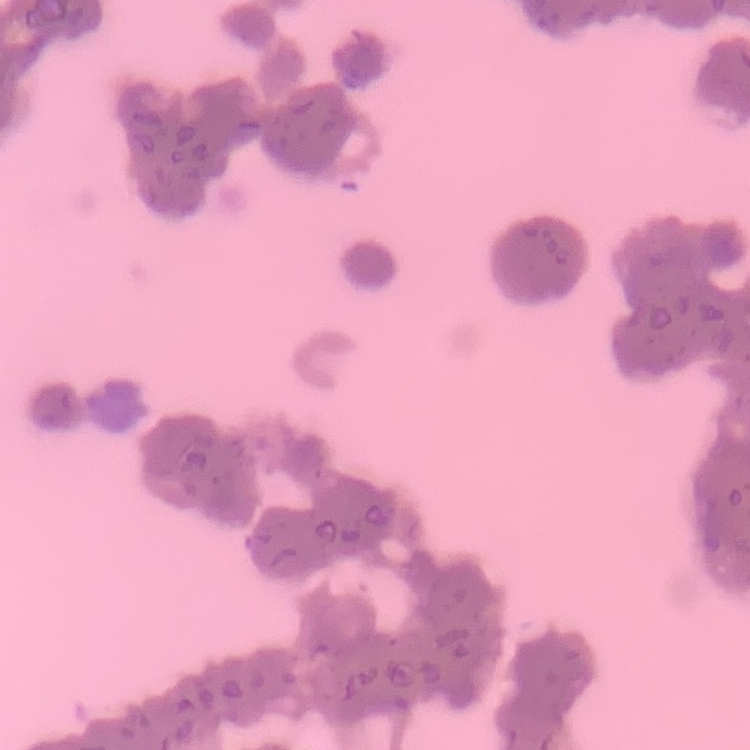

Summary:
  - Erythrocyte morphology: rouleaux formation
  - Stain: Field's or Giemsa
  - Image type: square crop of a larger photomicrograph
  - Preparation: thin blood film